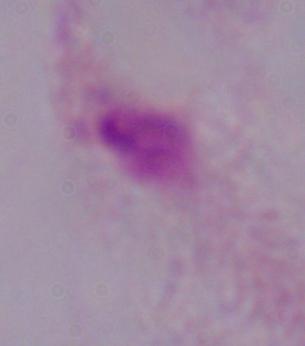
modality: photomicrograph
identification: trichomonad
magnification: 1000x